Classify this cell by malaria status.
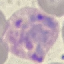
Parasitized.

stain: Giemsa
image_type: automatically extracted cell patch, resized to 64 × 64 pixels
preparation: thin blood film
capture: smartphone through the microscope eyepiece